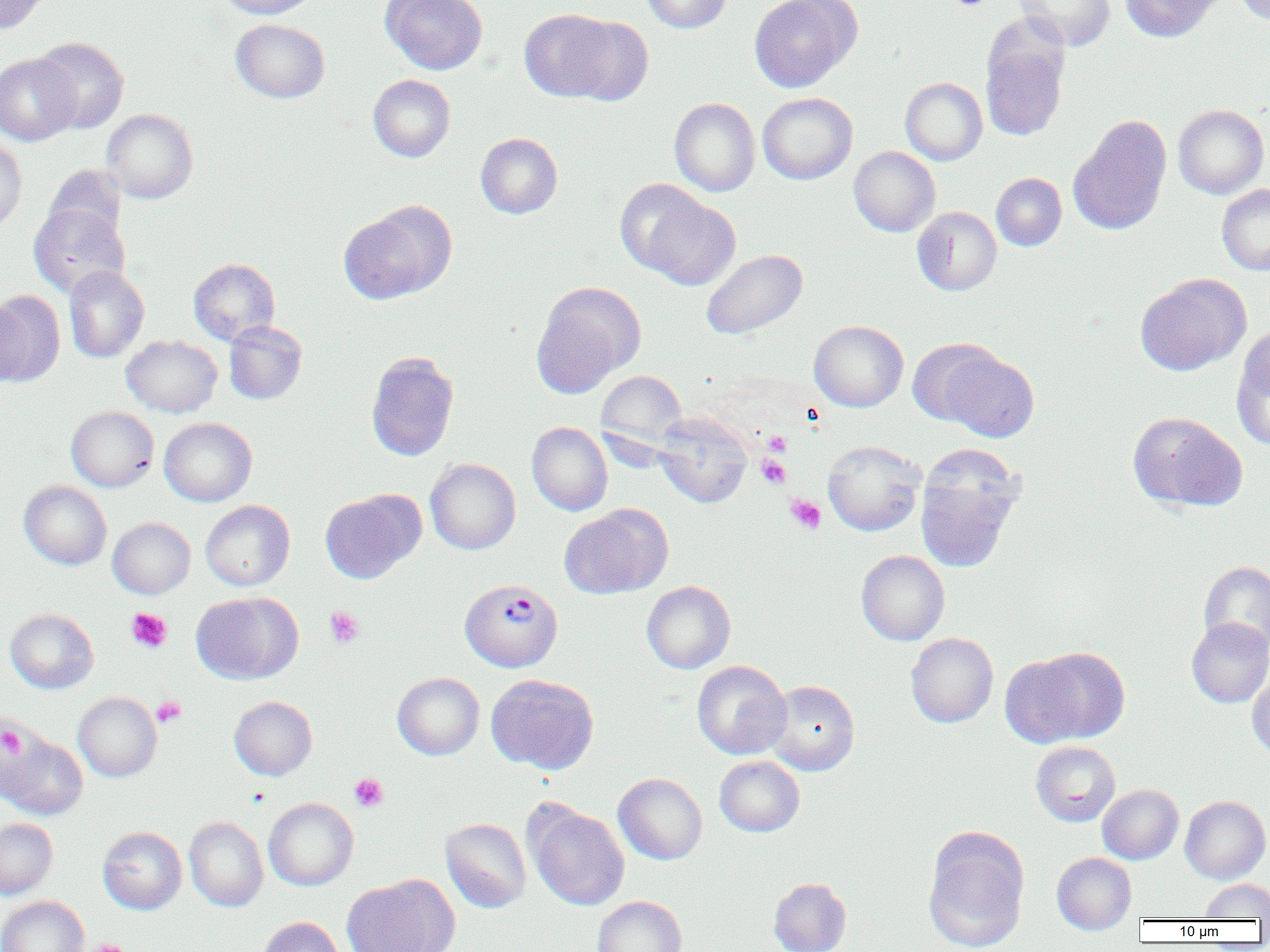

Approximate bounding boxes as named x1/y1/x2/y2 corners in pixels. Platelet locations: (x1=949, y1=0, x2=992, y2=11), (x1=764, y1=432, x2=791, y2=456), (x1=757, y1=454, x2=791, y2=489), (x1=786, y1=495, x2=826, y2=534), (x1=324, y1=606, x2=365, y2=648), (x1=126, y1=608, x2=172, y2=653), (x1=152, y1=697, x2=186, y2=727), (x1=1, y1=725, x2=25, y2=758), (x1=349, y1=773, x2=389, y2=812), (x1=89, y1=940, x2=130, y2=952). Uninfected red blood cell locations: (x1=0, y1=0, x2=51, y2=35), (x1=214, y1=0, x2=320, y2=18), (x1=380, y1=0, x2=487, y2=75), (x1=641, y1=0, x2=732, y2=33), (x1=749, y1=0, x2=862, y2=92), (x1=1015, y1=0, x2=1115, y2=50), (x1=1120, y1=0, x2=1222, y2=43), (x1=1234, y1=0, x2=1270, y2=25), (x1=519, y1=9, x2=624, y2=102), (x1=566, y1=16, x2=654, y2=105), (x1=231, y1=19, x2=330, y2=103), (x1=981, y1=34, x2=1069, y2=142), (x1=32, y1=37, x2=130, y2=134), (x1=0, y1=54, x2=80, y2=145), (x1=368, y1=74, x2=455, y2=162), (x1=900, y1=77, x2=987, y2=165), (x1=757, y1=92, x2=857, y2=184), (x1=669, y1=98, x2=760, y2=196), (x1=1173, y1=104, x2=1269, y2=199), (x1=101, y1=109, x2=198, y2=204), (x1=1068, y1=115, x2=1171, y2=236), (x1=475, y1=133, x2=563, y2=218), (x1=0, y1=139, x2=27, y2=234), (x1=849, y1=146, x2=940, y2=237), (x1=43, y1=164, x2=126, y2=246), (x1=991, y1=172, x2=1067, y2=251), (x1=1217, y1=184, x2=1270, y2=275), (x1=633, y1=191, x2=741, y2=290), (x1=339, y1=202, x2=455, y2=304), (x1=28, y1=204, x2=129, y2=298), (x1=912, y1=206, x2=1002, y2=295), (x1=701, y1=248, x2=808, y2=340), (x1=188, y1=258, x2=280, y2=346), (x1=63, y1=265, x2=149, y2=363), (x1=1135, y1=273, x2=1251, y2=376), (x1=531, y1=282, x2=645, y2=397), (x1=0, y1=290, x2=65, y2=385), (x1=0, y1=296, x2=30, y2=388), (x1=224, y1=320, x2=307, y2=404), (x1=808, y1=320, x2=909, y2=412), (x1=1233, y1=331, x2=1270, y2=448), (x1=121, y1=335, x2=221, y2=417), (x1=908, y1=337, x2=1007, y2=427), (x1=936, y1=346, x2=1039, y2=442), (x1=365, y1=351, x2=459, y2=462), (x1=595, y1=370, x2=688, y2=451), (x1=65, y1=406, x2=159, y2=492), (x1=653, y1=412, x2=752, y2=508), (x1=1128, y1=412, x2=1247, y2=512), (x1=158, y1=417, x2=257, y2=506), (x1=527, y1=421, x2=613, y2=516), (x1=822, y1=440, x2=925, y2=536), (x1=915, y1=452, x2=1023, y2=573), (x1=425, y1=458, x2=520, y2=554), (x1=19, y1=480, x2=111, y2=570), (x1=320, y1=489, x2=425, y2=584), (x1=200, y1=500, x2=295, y2=591), (x1=559, y1=504, x2=672, y2=599), (x1=108, y1=517, x2=195, y2=599), (x1=856, y1=550, x2=950, y2=645), (x1=1199, y1=561, x2=1270, y2=654), (x1=641, y1=580, x2=736, y2=673), (x1=190, y1=592, x2=302, y2=684), (x1=5, y1=609, x2=99, y2=694), (x1=1186, y1=617, x2=1270, y2=707), (x1=905, y1=632, x2=998, y2=727), (x1=1003, y1=646, x2=1130, y2=747), (x1=692, y1=660, x2=792, y2=760), (x1=1247, y1=671, x2=1270, y2=761), (x1=392, y1=672, x2=484, y2=760), (x1=486, y1=673, x2=599, y2=774), (x1=765, y1=680, x2=860, y2=775), (x1=73, y1=692, x2=162, y2=782), (x1=229, y1=696, x2=317, y2=780), (x1=1, y1=729, x2=88, y2=821), (x1=1030, y1=741, x2=1120, y2=827), (x1=714, y1=755, x2=805, y2=837), (x1=613, y1=772, x2=707, y2=865), (x1=1097, y1=784, x2=1183, y2=864), (x1=1180, y1=795, x2=1270, y2=884), (x1=263, y1=797, x2=359, y2=891), (x1=525, y1=802, x2=630, y2=911), (x1=184, y1=816, x2=268, y2=912), (x1=0, y1=818, x2=57, y2=900), (x1=440, y1=818, x2=531, y2=913), (x1=97, y1=826, x2=187, y2=915), (x1=923, y1=828, x2=1029, y2=952), (x1=1051, y1=852, x2=1136, y2=935), (x1=342, y1=874, x2=459, y2=952), (x1=768, y1=877, x2=851, y2=952), (x1=1201, y1=879, x2=1270, y2=919), (x1=0, y1=895, x2=89, y2=952), (x1=592, y1=896, x2=686, y2=952), (x1=257, y1=916, x2=346, y2=952). Plasmodium vivax-infected red blood cell locations: (x1=460, y1=579, x2=563, y2=673). Slide-level diagnosis: Plasmodium vivax. Captured at 1000x magnification. Thin blood smear. Light microscopy. One field of a larger specimen. Image is 1270×952 pixels.